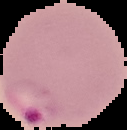
malaria status = parasitized
image size = 127×130 pixels
image type = segmented cell region with the area outside set to black
preparation = thin blood smear